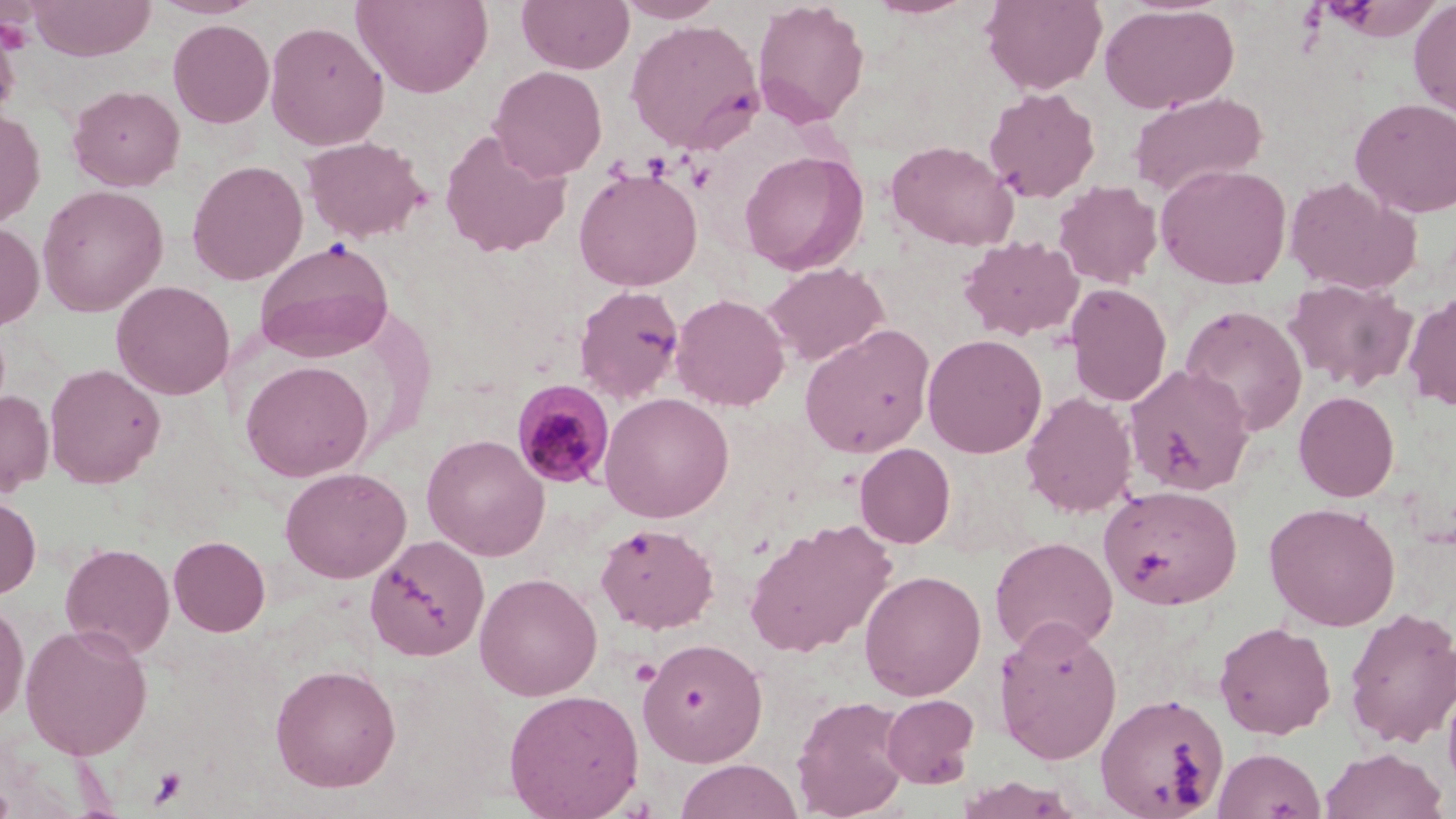

Summary:
  - Coordinate format: approximate bounding boxes as [x1, y1, x2, y2] in pixels
  - Plasmodium malariae-infected red blood cell locations: [512, 380, 616, 490]
  - Uninfected red blood cell locations: [28, 0, 155, 61], [149, 0, 264, 19], [516, 0, 634, 73], [615, 0, 726, 23], [751, 0, 870, 129], [864, 0, 981, 19], [981, 0, 1108, 94], [352, 1, 493, 98], [1328, 1, 1444, 42], [1409, 2, 1456, 119], [1099, 3, 1239, 115], [0, 18, 21, 123], [625, 18, 764, 153], [168, 19, 275, 128], [264, 20, 389, 151], [489, 65, 607, 181], [68, 84, 185, 191], [983, 87, 1100, 204], [1128, 90, 1268, 200], [1349, 97, 1456, 218], [0, 108, 45, 228], [439, 129, 572, 259], [302, 135, 429, 243], [885, 140, 1018, 251], [739, 150, 869, 274], [187, 159, 308, 285], [1155, 163, 1292, 289], [573, 167, 703, 291], [1283, 176, 1421, 295], [1052, 181, 1163, 288], [37, 185, 169, 317], [0, 221, 44, 330], [958, 235, 1085, 341], [254, 238, 394, 362], [763, 262, 889, 366], [1282, 278, 1417, 392], [111, 280, 235, 400], [1064, 283, 1173, 407], [573, 284, 686, 405], [1403, 291, 1456, 412], [671, 293, 790, 411], [1179, 304, 1308, 437], [799, 324, 936, 458], [922, 333, 1047, 458], [240, 360, 374, 482], [44, 363, 166, 488], [1124, 364, 1256, 497], [0, 390, 54, 496], [1020, 390, 1138, 518], [1293, 391, 1399, 502], [599, 392, 734, 523], [422, 433, 550, 561], [854, 443, 956, 548], [280, 467, 411, 583], [1099, 484, 1242, 609], [0, 494, 41, 599], [1264, 501, 1401, 631], [745, 519, 897, 658], [596, 522, 719, 634], [365, 534, 490, 661], [168, 535, 270, 636], [990, 536, 1118, 656], [60, 542, 175, 659], [859, 569, 987, 701], [474, 572, 603, 701], [0, 599, 29, 724], [1343, 607, 1456, 750], [993, 616, 1123, 764], [1214, 621, 1337, 739], [20, 622, 153, 760], [638, 638, 769, 767], [269, 663, 402, 793], [1442, 678, 1456, 797], [503, 689, 645, 818], [1095, 693, 1230, 818], [880, 694, 979, 788], [791, 696, 910, 818], [1213, 747, 1326, 819], [1320, 747, 1448, 819], [675, 759, 802, 818]
  - Platelet locations: [1, 7, 36, 52], [686, 160, 716, 193], [629, 656, 662, 688], [148, 767, 187, 807]
  - Slide-level diagnosis: Plasmodium malariae
  - Modality: optical microscopy
  - Field of view: one of a larger specimen
  - Preparation: thin blood smear
  - Image size: 1456×819 pixels
  - Stain: May-Grünwald-Giemsa
  - Magnification: 1000x